Point out malaria parasites and leukocytes.
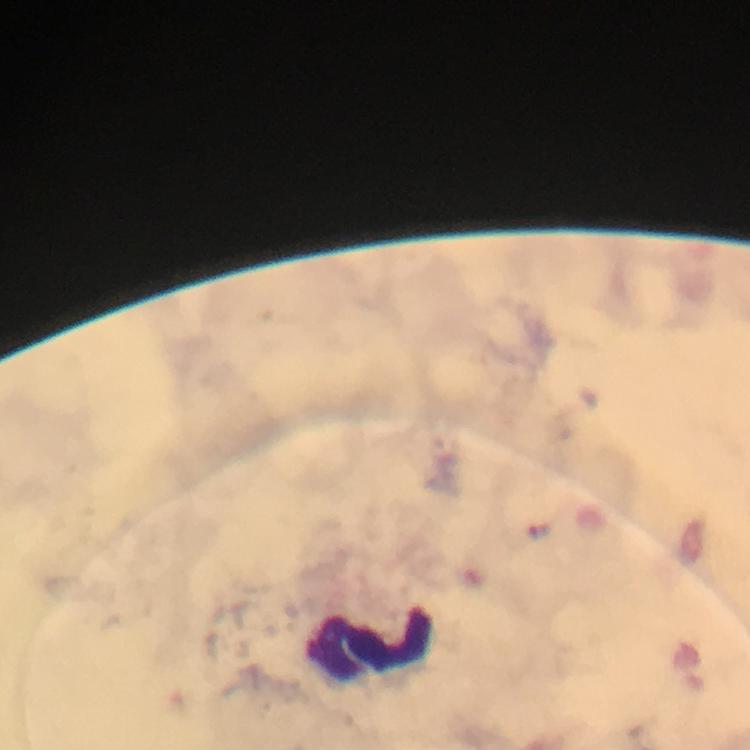

No malaria parasites detected.
Approximate centers as [x, y] in pixels.
Leukocytes: [368, 644].

From a malaria diagnostic workup. 100x magnification. Image is 750×750 pixels. Immersion oil applied. Cropped region of a single field of view. Giemsa-stained preparation. Smartphone photograph taken through a microscope. Thick blood film.